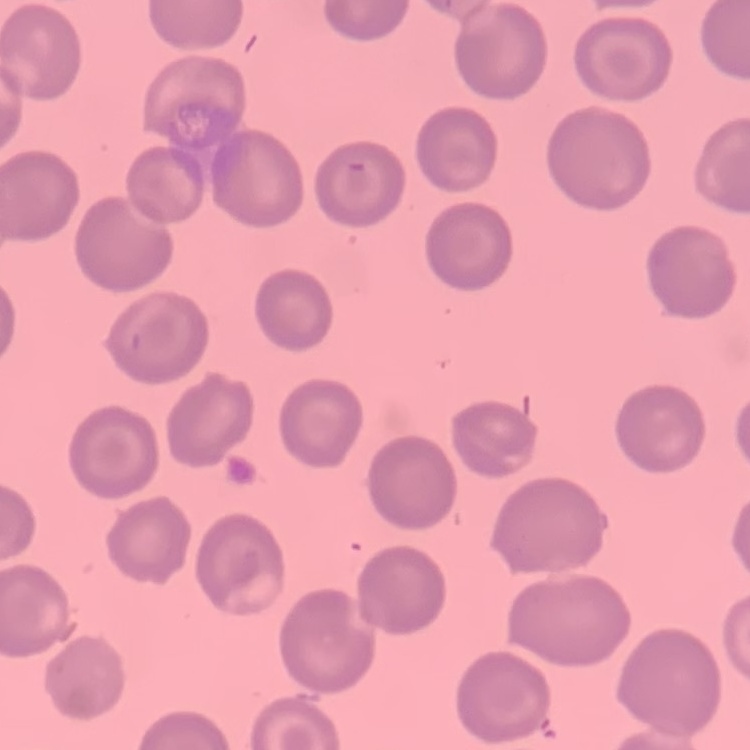

erythrocyte morphology = no rouleaux formation
image type = square crop of a larger photomicrograph
stain = Field's or Giemsa
preparation = thin peripheral smear